Assess this cell for malaria.
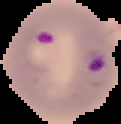

It is parasitized.

preparation = thin blood film
image size = 121×124 pixels
image type = cell region segmented out of the field of view; surrounding area masked to black